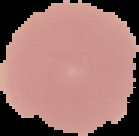
preparation = thin blood smear
image type = cell region segmented out of the field of view; surrounding area masked to black
result = negative for Plasmodium parasites
image size = 139×136 pixels